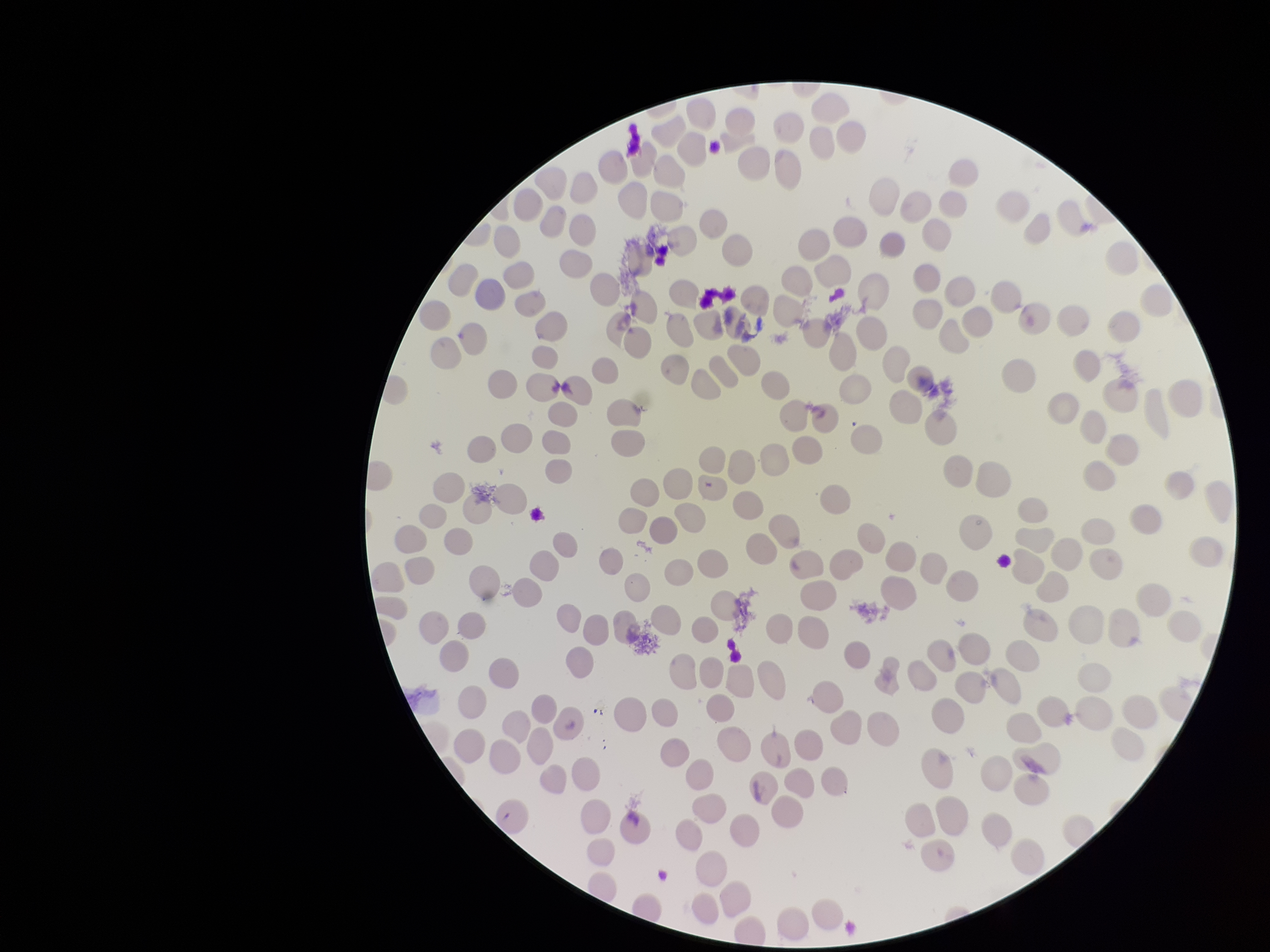
Photographed through the microscope eyepiece with a smartphone camera. Red blood cell count: 190. Preparation: thin. Parasitized red blood cells: none detected. Patient malaria status: negative. Single field of view. Parasitized red blood cell count: 0. Stained with Giemsa. Image is 1270×952 pixels.